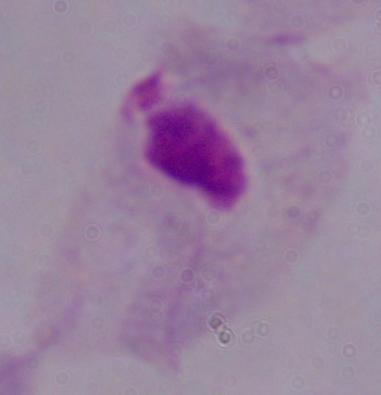 Micrograph. Captured at 1000x magnification. A trichomonad is seen.